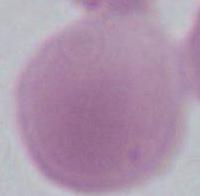 Captured at 1000x magnification. Photomicrograph. An erythrocyte is seen.